Classify this cell by malaria status.
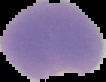

It is parasitized.

Summary:
  - Image size: 106×82 pixels
  - Preparation: thin blood smear
  - Image type: cell region segmented out of the field of view; surrounding area masked to black